Identify the preparation type.
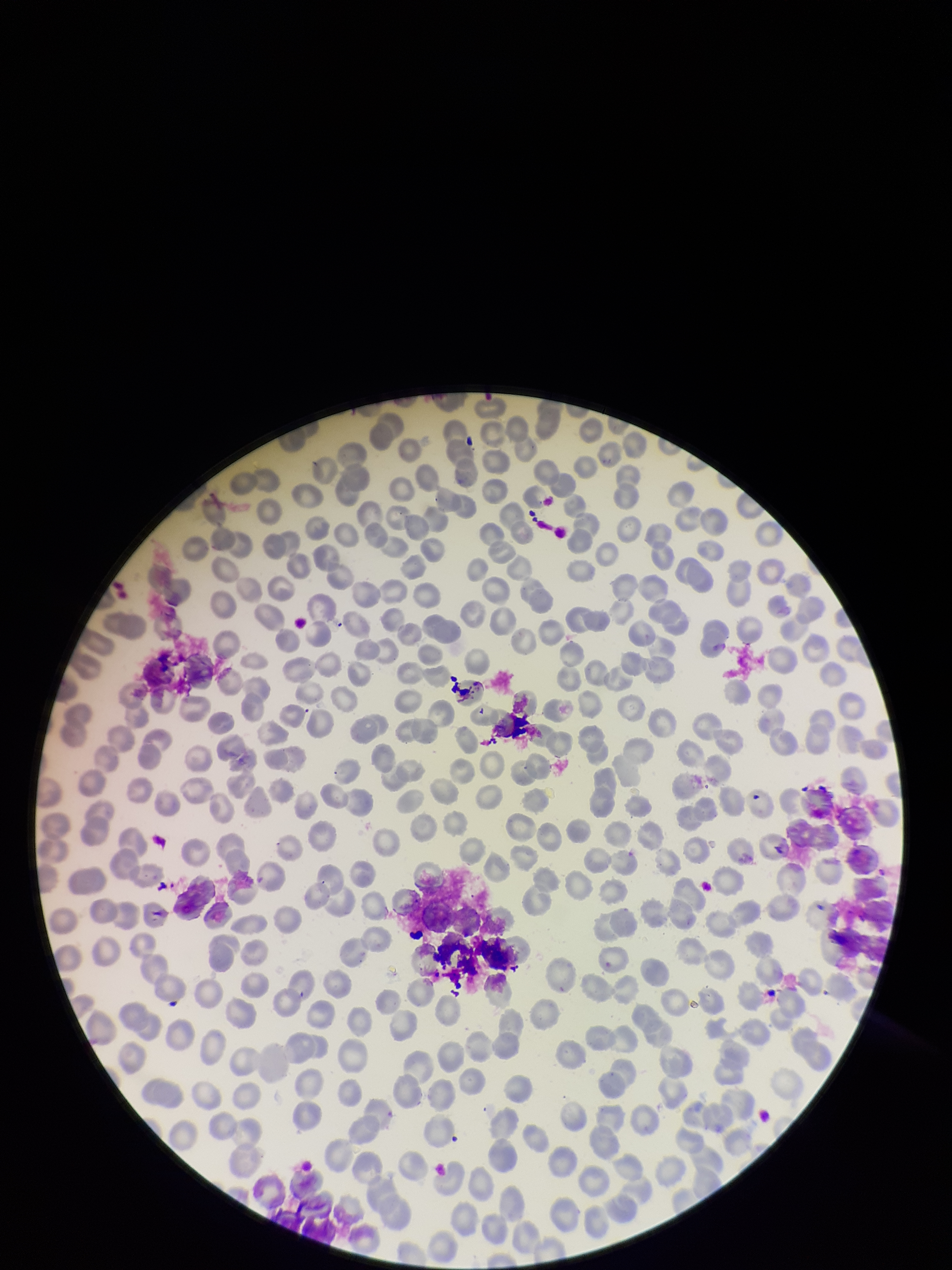
It is a thin blood smear.

red blood cell count = 221
patient malaria status = negative
capture = smartphone photograph through the microscope eyepiece
parasitized red blood cells = none seen
parasitized red blood cell count = 0
stain = Giemsa
image size = 952×1270 pixels
field of view = one from this slide